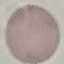

{
  "result": "no malaria parasites detected",
  "image_type": "cell patch, automatically extracted from a larger field of view and resized to 64 × 64 pixels",
  "capture": "smartphone camera at the microscope eyepiece",
  "stain": "Giemsa",
  "preparation": "thin blood film"
}